Classify this cell by malaria status.
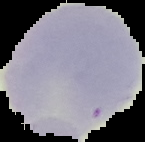

It is uninfected.

{
  "image_type": "segmented cell region with the area outside set to black",
  "preparation": "thin blood smear",
  "image_size": "145×142 pixels"
}